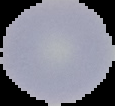 Image is 115×106 pixels. From a thin blood smear. The area outside the segmented cell region is set to black. Result: no Plasmodium parasites detected.